Locate every uninfected red blood cell.
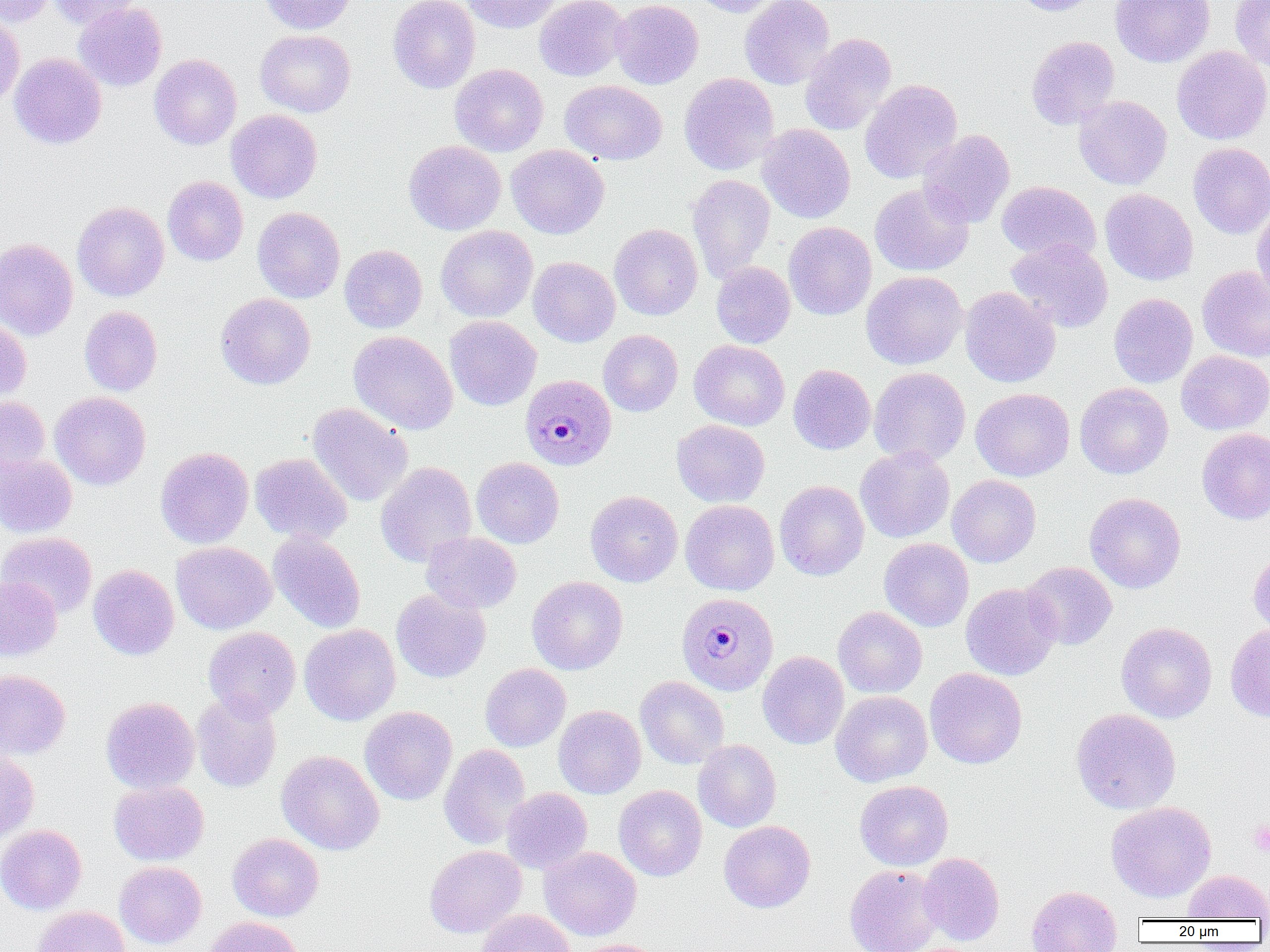

Approximate bounding boxes as [x1, y1, x2, y2] in pixels.
Uninfected red blood cells: [1, 0, 53, 27], [48, 0, 139, 29], [259, 0, 356, 34], [388, 0, 480, 93], [460, 0, 563, 33], [534, 0, 629, 81], [610, 0, 704, 89], [689, 0, 784, 17], [739, 0, 835, 89], [1012, 0, 1101, 16], [1110, 0, 1215, 67], [1230, 0, 1270, 70], [74, 3, 167, 92], [0, 12, 25, 109], [255, 29, 356, 118], [799, 33, 897, 136], [1026, 36, 1120, 130], [1171, 45, 1270, 145], [9, 53, 106, 149], [149, 54, 242, 150], [450, 64, 548, 156], [679, 73, 779, 175], [860, 79, 963, 184], [560, 80, 667, 165], [1074, 95, 1172, 190], [226, 109, 322, 203], [756, 124, 855, 223], [918, 129, 1015, 228], [404, 140, 506, 235], [1188, 143, 1270, 239], [506, 144, 609, 239], [687, 174, 776, 282], [162, 176, 248, 265], [997, 181, 1101, 263], [870, 183, 974, 277], [1100, 188, 1198, 286], [72, 200, 169, 301], [1252, 204, 1270, 303], [252, 207, 345, 303], [784, 222, 876, 320], [609, 223, 703, 320], [435, 225, 538, 322], [0, 238, 79, 341], [1005, 239, 1113, 333], [339, 245, 427, 333], [528, 256, 620, 347], [711, 261, 795, 348], [1197, 265, 1270, 363], [861, 271, 967, 370], [960, 287, 1060, 387], [215, 293, 315, 389], [1108, 293, 1197, 388], [79, 306, 162, 395], [444, 316, 541, 411], [0, 317, 31, 406], [348, 330, 458, 434], [598, 330, 683, 417], [689, 340, 790, 431], [1176, 350, 1270, 435], [788, 364, 876, 454], [869, 367, 971, 466], [1075, 383, 1173, 479], [970, 388, 1075, 481], [50, 391, 151, 490], [0, 397, 51, 477], [307, 403, 413, 506], [672, 420, 770, 507], [1196, 428, 1270, 525], [155, 446, 254, 548], [854, 447, 955, 543], [250, 453, 352, 545], [0, 454, 77, 537], [471, 457, 564, 548], [376, 461, 477, 567], [947, 474, 1041, 567], [775, 480, 869, 580], [585, 490, 682, 587], [1084, 492, 1186, 593], [680, 500, 779, 595], [268, 531, 365, 633], [0, 532, 97, 618], [422, 532, 522, 613], [879, 538, 973, 632], [171, 541, 276, 634], [1248, 549, 1270, 638], [1022, 561, 1117, 650], [88, 564, 179, 660], [0, 576, 62, 661], [527, 576, 628, 675], [961, 583, 1061, 681], [391, 588, 491, 683], [833, 606, 927, 698], [1116, 622, 1217, 723], [299, 624, 400, 725], [1225, 624, 1270, 723], [203, 627, 300, 720], [758, 651, 849, 749], [480, 663, 570, 751], [925, 667, 1027, 769], [0, 669, 71, 758], [635, 676, 729, 769], [192, 691, 281, 792], [831, 691, 932, 787], [101, 696, 200, 793], [360, 705, 457, 805], [553, 705, 646, 798], [1071, 708, 1181, 814], [693, 739, 781, 832], [439, 744, 531, 849], [276, 750, 384, 855], [0, 751, 39, 844], [854, 780, 953, 871], [109, 781, 209, 866], [614, 785, 707, 881], [502, 787, 592, 873], [1106, 801, 1216, 902], [718, 820, 816, 912], [0, 824, 87, 914], [227, 833, 324, 921], [424, 845, 526, 937], [540, 846, 641, 941], [918, 852, 1004, 945], [114, 861, 206, 949], [845, 864, 945, 952], [1182, 870, 1270, 920], [1027, 885, 1122, 952], [33, 906, 131, 952], [477, 909, 576, 952], [205, 916, 302, 952], [573, 939, 669, 952].

Plasmodium malariae-infected red blood cell locations: [520, 375, 617, 470], [677, 592, 778, 695]. Platelet locations: [1248, 819, 1270, 856]. Slide-level diagnosis: Plasmodium malariae. Captured at 1000x magnification. Image is 1270×952 pixels. Thin blood film. One field of a larger specimen. Light microscopy.